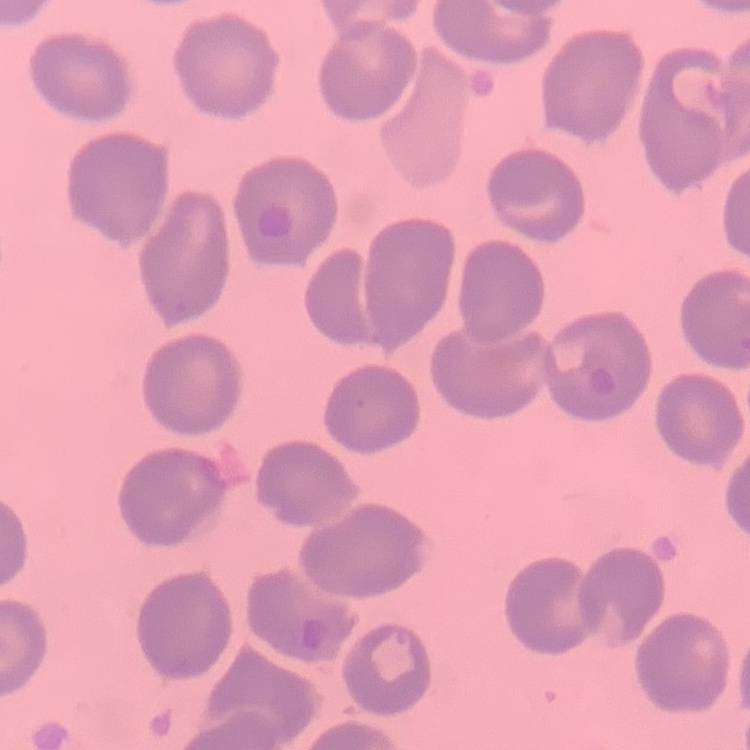
Summary:
  - Erythrocyte morphology: no rouleaux formation
  - Preparation: thin peripheral smear
  - Stain: Field's or Giemsa
  - Image type: one tile cut from a larger photomicrograph